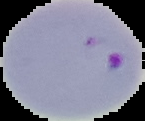
image size = 145×121 pixels
preparation = thin blood smear
image type = segmented cell region on a black background
malaria status = parasitized